Assess this cell for malaria.
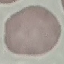
It is uninfected.

Acquired by smartphone through the microscope eyepiece. Thin blood smear. Giemsa stain. Automatically extracted cell patch, resized to 64 × 64 pixels.